Name the blood parasite species.
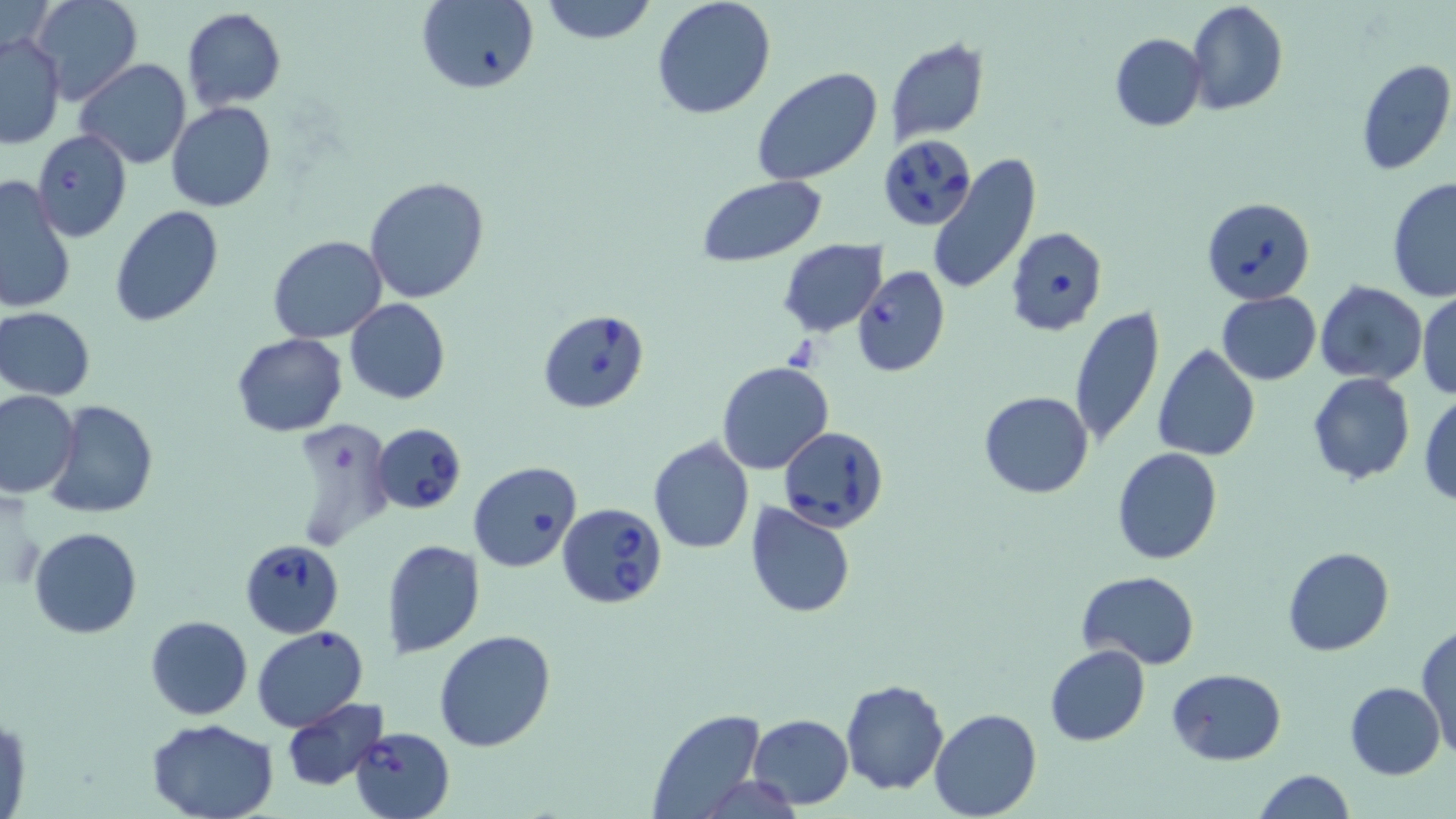
Babesia divergens.

field of view = single
Babesia divergens-infected red blood cell locations = approximate bounding boxes as [x1, y1, x2, y2] in pixels: [881, 134, 977, 231], [1203, 197, 1315, 305], [1005, 226, 1108, 337], [850, 265, 950, 377], [538, 309, 651, 414], [372, 422, 467, 515], [779, 425, 889, 531], [557, 503, 668, 609], [240, 538, 344, 637], [353, 725, 456, 819]
image size = 1456×819 pixels
modality = optical microscopy
magnification = 1000x
stain = May-Grünwald-Giemsa
preparation = thin blood film
uninfected red blood cell locations = approximate bounding boxes as [x1, y1, x2, y2] in pixels: [3, 0, 54, 54], [31, 0, 142, 106], [415, 0, 539, 95], [540, 0, 656, 45], [652, 0, 777, 120], [1186, 1, 1289, 116], [181, 8, 286, 109], [0, 32, 66, 150], [1109, 33, 1206, 132], [886, 37, 989, 142], [75, 58, 191, 169], [1355, 58, 1456, 176], [753, 66, 883, 187], [167, 102, 276, 214], [31, 129, 132, 242], [925, 153, 1041, 296], [1, 175, 75, 314], [364, 176, 490, 304], [695, 176, 827, 268], [1387, 176, 1455, 305], [109, 205, 224, 327], [267, 235, 387, 344], [778, 239, 886, 337], [1313, 281, 1426, 385], [1216, 291, 1322, 384], [1416, 291, 1456, 402], [345, 300, 451, 404], [1067, 306, 1167, 451], [0, 307, 95, 402], [230, 333, 346, 437], [1152, 344, 1261, 461], [716, 361, 833, 474], [1306, 374, 1416, 485], [0, 390, 80, 498], [977, 391, 1094, 498], [1419, 393, 1456, 507], [45, 400, 159, 519], [285, 417, 393, 550], [649, 438, 754, 554], [1113, 448, 1223, 564], [468, 462, 583, 571], [745, 503, 855, 618], [29, 527, 142, 639], [382, 539, 484, 658], [1281, 546, 1394, 655], [1077, 571, 1200, 667], [145, 614, 253, 721], [1416, 624, 1456, 763], [251, 626, 371, 731], [434, 629, 558, 751], [1045, 645, 1150, 746], [1168, 669, 1286, 765], [840, 679, 948, 796], [1345, 683, 1445, 780], [282, 698, 389, 791], [1, 708, 29, 819], [930, 708, 1041, 819], [646, 709, 765, 819], [747, 713, 853, 809], [147, 718, 280, 819], [1251, 768, 1356, 819]